Report the malaria status of this cell.
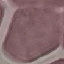
Uninfected.

image_type: cell patch, automatically extracted from a larger field of view and resized to 64 × 64 pixels
capture: smartphone camera at the microscope eyepiece
stain: Giemsa
preparation: thin blood film